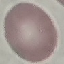

{
  "malaria_status": "uninfected",
  "stain": "Giemsa",
  "preparation": "thin blood smear",
  "image_type": "automatically extracted cell patch, resized to 64 × 64 pixels",
  "capture": "smartphone camera at the microscope eyepiece"
}